Name the blood parasite species.
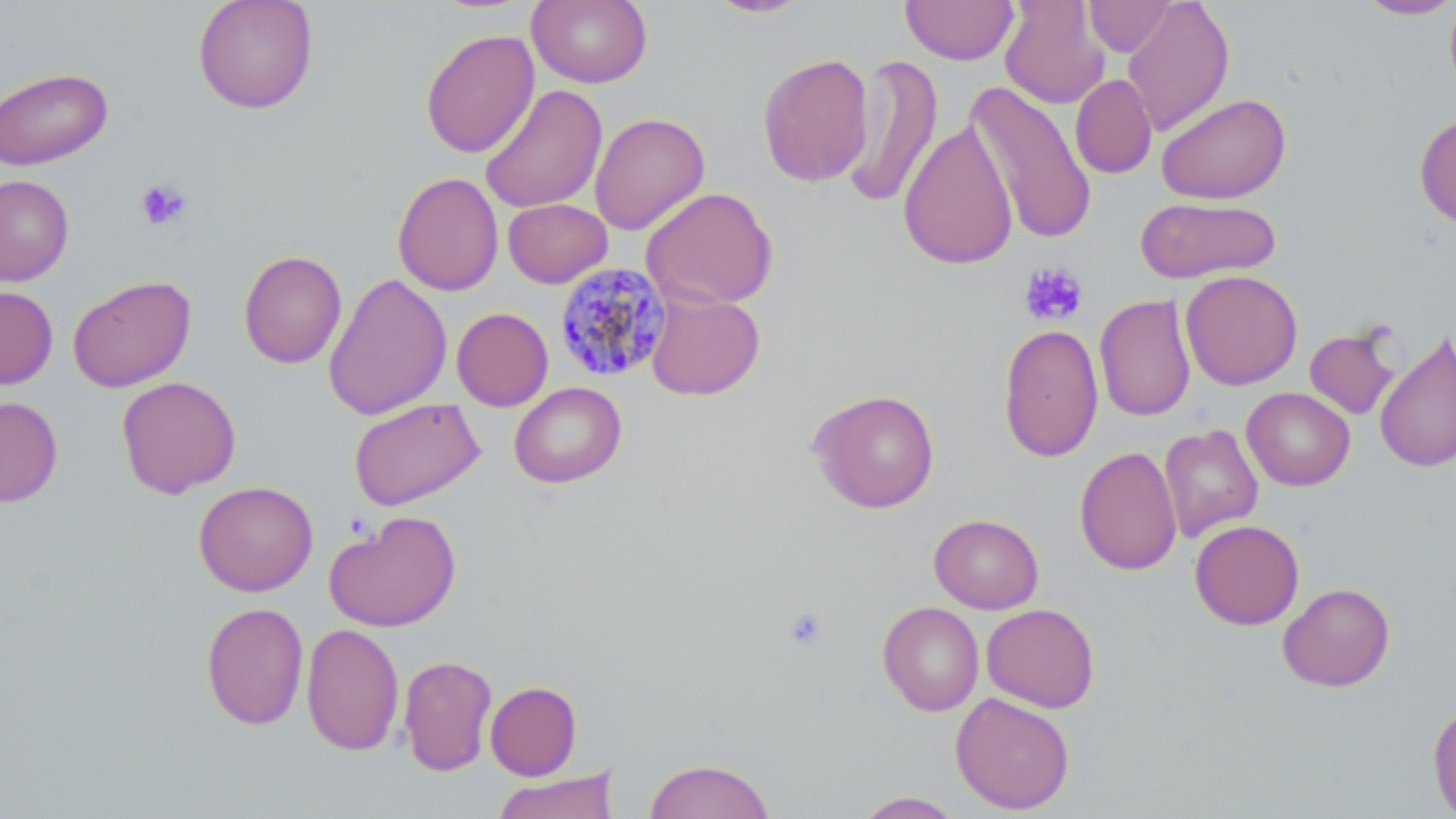

Plasmodium malariae.

Approximate bounding boxes as [x1, y1, x2, y2] in pixels. Uninfected red blood cell locations: [192, 0, 319, 114], [527, 0, 652, 88], [702, 0, 814, 19], [900, 0, 1019, 65], [1083, 0, 1178, 57], [1121, 0, 1235, 137], [999, 1, 1111, 109], [1355, 1, 1456, 20], [1445, 1, 1456, 102], [420, 28, 540, 158], [757, 52, 874, 188], [841, 53, 943, 210], [0, 66, 113, 170], [1070, 73, 1157, 179], [964, 81, 1099, 245], [479, 85, 608, 213], [1156, 92, 1291, 204], [589, 112, 710, 235], [1415, 112, 1456, 230], [898, 120, 1018, 271], [392, 172, 504, 296], [0, 175, 74, 286], [641, 187, 778, 310], [1136, 195, 1281, 284], [503, 198, 613, 288], [238, 250, 348, 369], [1180, 269, 1303, 390], [323, 272, 452, 421], [68, 275, 196, 392], [0, 286, 58, 389], [645, 290, 765, 400], [1094, 293, 1196, 421], [451, 307, 553, 411], [998, 323, 1103, 463], [1305, 324, 1401, 420], [1374, 331, 1456, 474], [116, 376, 241, 498], [509, 382, 627, 488], [1242, 387, 1356, 490], [808, 388, 941, 513], [0, 396, 63, 507], [349, 398, 485, 510], [1158, 423, 1263, 542], [1075, 446, 1182, 575], [193, 480, 318, 596], [324, 510, 461, 632], [929, 513, 1044, 614], [1189, 519, 1304, 629], [1277, 581, 1395, 692], [201, 601, 309, 730], [877, 601, 984, 716], [981, 603, 1100, 713], [301, 622, 404, 757], [398, 654, 497, 777], [485, 681, 582, 780], [950, 691, 1075, 814], [1427, 699, 1456, 818], [643, 757, 777, 819], [491, 769, 618, 819], [852, 790, 966, 818]. Plasmodium malariae-infected red blood cell locations: [554, 262, 674, 384]. Platelet locations: [134, 178, 192, 231], [1019, 262, 1089, 327], [782, 606, 828, 651]. Image is 1456×819 pixels. May-Grünwald-Giemsa-stained preparation. 1000x magnification. Thin blood film. Single field of view. Light microscopy.